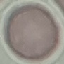 Result: negative for malaria parasites. Thin blood film. Cell patch, automatically extracted from a larger field of view and resized to 64 × 64 pixels. Photographed with a smartphone camera at the microscope eyepiece. Giemsa-stained preparation.